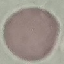
Summary:
  - Result: negative for malaria parasites
  - Capture: smartphone through the microscope eyepiece
  - Stain: Giemsa
  - Image type: cell patch, automatically extracted from a larger field of view and resized to 64 × 64 pixels
  - Preparation: thin blood film